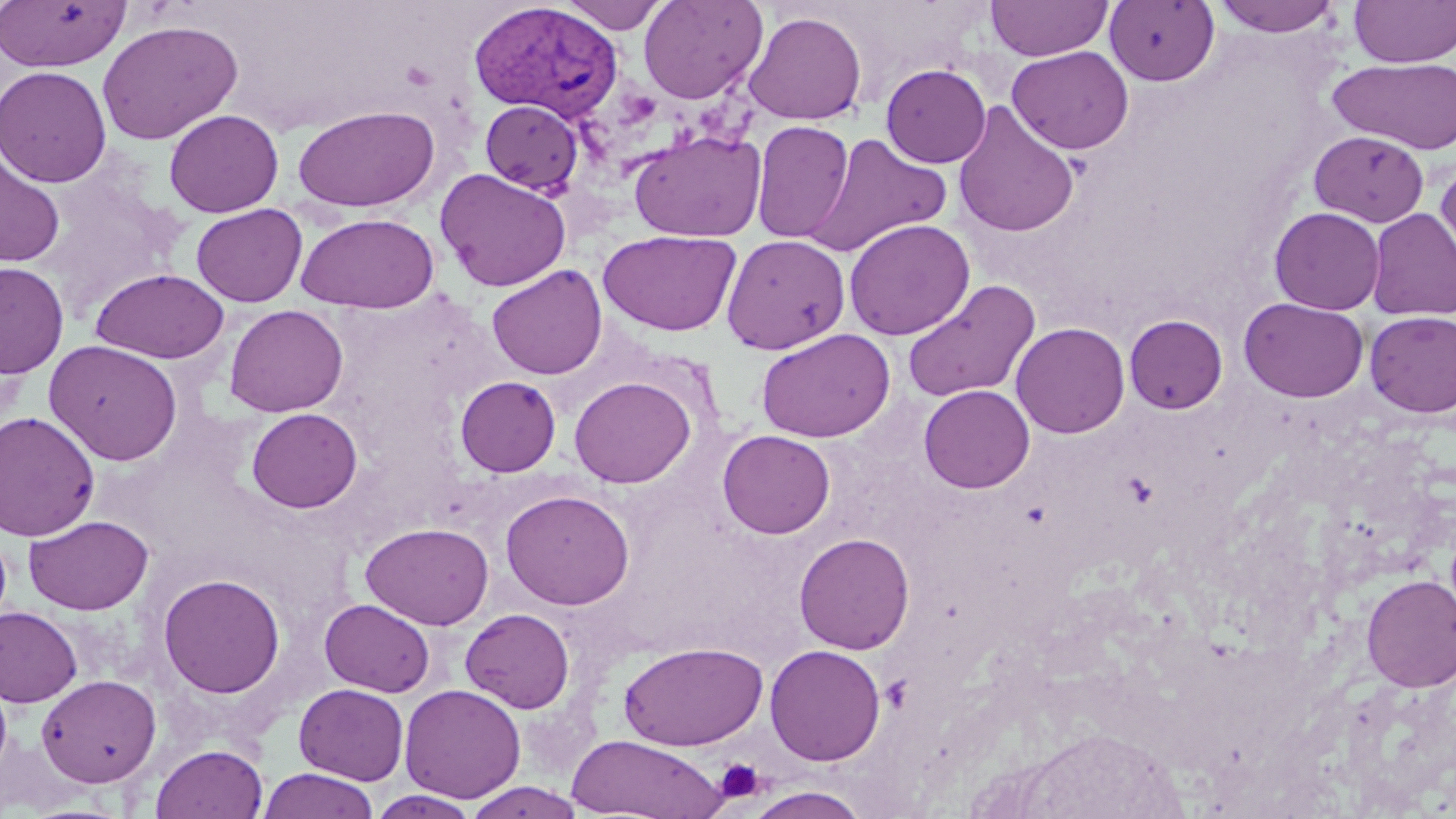
slide-level diagnosis = Plasmodium vivax
modality = light microscopy
platelet locations = approximate bounding boxes as [x1, y1, x2, y2] in pixels: [400, 61, 437, 90], [714, 758, 765, 804]
magnification = 1000x
preparation = thin blood smear
stain = May-Grünwald-Giemsa
image size = 1456×819 pixels
uninfected red blood cell locations = approximate bounding boxes as [x1, y1, x2, y2] in pixels: [0, 0, 130, 72], [638, 0, 767, 104], [985, 0, 1113, 61], [1105, 0, 1219, 86], [1210, 0, 1344, 38], [1350, 0, 1456, 67], [559, 1, 670, 33], [743, 10, 868, 125], [97, 20, 243, 144], [1006, 46, 1134, 154], [1328, 57, 1456, 154], [881, 63, 991, 167], [0, 65, 112, 187], [480, 100, 584, 195], [952, 103, 1079, 238], [293, 105, 440, 212], [164, 109, 284, 217], [751, 120, 854, 243], [629, 129, 767, 242], [1309, 130, 1429, 226], [803, 133, 952, 256], [0, 154, 65, 267], [1436, 159, 1456, 278], [435, 168, 572, 291], [191, 203, 307, 307], [1269, 206, 1385, 314], [1367, 208, 1456, 321], [296, 213, 439, 313], [844, 218, 975, 341], [599, 229, 741, 336], [721, 234, 850, 354], [0, 262, 69, 378], [486, 264, 607, 380], [91, 268, 229, 363], [902, 279, 1041, 401], [1239, 298, 1368, 403], [224, 304, 348, 417], [1364, 311, 1456, 417], [1124, 314, 1228, 414], [1011, 322, 1130, 438], [757, 328, 895, 442], [45, 340, 183, 465], [569, 374, 696, 488], [455, 375, 561, 476], [919, 384, 1035, 493], [246, 407, 363, 513], [0, 411, 101, 541], [717, 429, 835, 538], [500, 488, 635, 610], [24, 515, 154, 614], [360, 522, 493, 629], [794, 533, 915, 654], [157, 572, 286, 699], [1361, 574, 1456, 691], [320, 599, 435, 697], [0, 606, 83, 708], [460, 608, 575, 713], [619, 641, 768, 750], [764, 644, 886, 765], [36, 674, 161, 787], [293, 683, 410, 784], [399, 683, 526, 803], [1015, 728, 1179, 819], [566, 734, 727, 818], [151, 743, 267, 819], [257, 768, 380, 819], [462, 782, 586, 819], [745, 787, 872, 818], [368, 790, 483, 818]
Plasmodium vivax-infected red blood cell locations = approximate bounding boxes as [x1, y1, x2, y2] in pixels: [468, 3, 624, 123]
field of view = one of a larger specimen